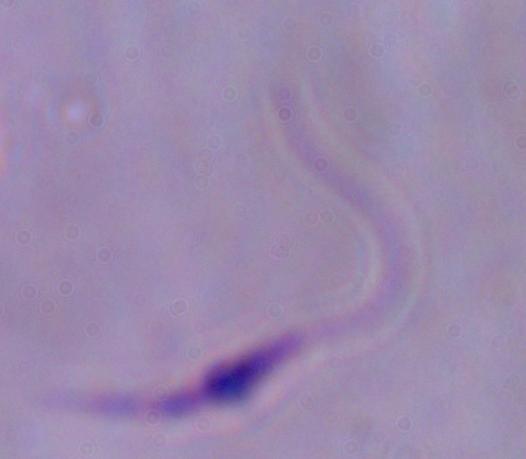
{
  "magnification": "1000x",
  "identification": "Leishmania",
  "modality": "photomicrograph"
}